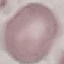
result = no malaria parasites seen
image type = cell patch, automatically extracted from a larger field of view and resized to 64 × 64 pixels
capture = smartphone through the microscope eyepiece
stain = Giemsa
preparation = thin blood smear